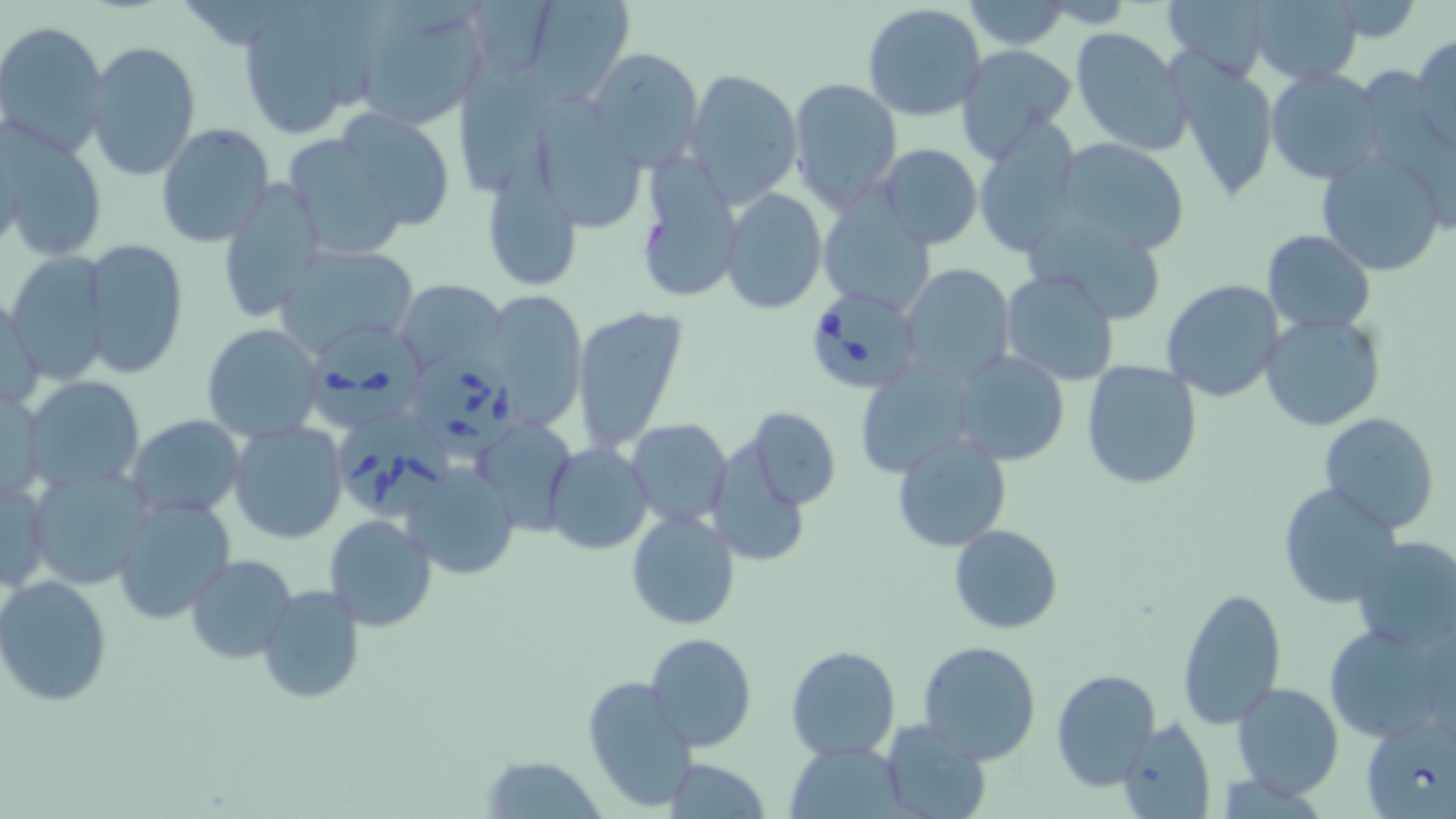

Summary:
  - Coordinate format: approximate bounding boxes as (x1, y1, x2, y2) in pixels
  - Babesia divergens-infected red blood cell locations: (801, 286, 922, 399), (307, 319, 426, 431), (411, 344, 523, 461), (336, 407, 453, 519)
  - Uninfected red blood cell locations: (350, 0, 493, 130), (517, 0, 630, 104), (1160, 0, 1275, 78), (1246, 0, 1363, 85), (235, 1, 380, 138), (964, 1, 1073, 49), (1325, 1, 1424, 45), (862, 3, 987, 122), (0, 21, 111, 158), (1070, 28, 1191, 152), (1411, 34, 1456, 152), (83, 40, 201, 182), (952, 44, 1077, 160), (584, 47, 703, 171), (1168, 53, 1281, 205), (683, 70, 802, 205), (1264, 70, 1384, 184), (787, 76, 903, 210), (334, 109, 456, 231), (154, 123, 274, 249), (1, 124, 108, 261), (971, 124, 1084, 255), (283, 135, 411, 259), (1053, 139, 1191, 256), (877, 145, 983, 249), (1316, 146, 1447, 277), (634, 154, 743, 307), (480, 170, 587, 294), (214, 179, 327, 324), (719, 188, 825, 314), (817, 194, 937, 317), (1025, 212, 1172, 325), (1261, 230, 1375, 335), (78, 239, 189, 378), (274, 243, 418, 359), (3, 249, 111, 382), (901, 262, 1016, 385), (1001, 269, 1119, 387), (393, 279, 506, 375), (1161, 279, 1285, 403), (482, 288, 589, 426), (1, 290, 46, 416), (572, 307, 689, 457), (1259, 311, 1386, 431), (201, 323, 324, 443), (949, 349, 1070, 466), (852, 360, 984, 479), (1081, 360, 1204, 488), (22, 376, 146, 492), (1, 388, 47, 502), (742, 407, 841, 510), (1319, 412, 1440, 534), (124, 413, 247, 520), (473, 414, 579, 531), (625, 418, 733, 527), (226, 420, 349, 545), (892, 431, 1010, 553), (543, 442, 654, 556), (704, 444, 815, 566), (401, 462, 521, 581), (28, 466, 156, 591), (1, 471, 53, 596), (1277, 482, 1403, 608), (357, 493, 506, 617), (109, 498, 237, 625), (626, 511, 741, 629), (323, 513, 438, 632), (949, 524, 1063, 634), (1350, 537, 1456, 652), (186, 554, 298, 666), (0, 575, 117, 706), (256, 583, 367, 705), (1176, 586, 1286, 729), (1323, 621, 1454, 744), (646, 632, 756, 750), (916, 640, 1042, 765), (785, 644, 901, 762), (1049, 670, 1161, 790), (582, 676, 696, 812), (1232, 682, 1344, 798), (1115, 717, 1217, 819), (877, 719, 991, 819), (789, 742, 903, 817), (482, 756, 605, 816), (662, 758, 772, 817)
  - Slide-level diagnosis: Babesia divergens
  - Modality: optical microscopy
  - Image size: 1456×819 pixels
  - Stain: May-Grünwald-Giemsa
  - Preparation: thin blood film
  - Field of view: one of a larger specimen
  - Magnification: 1000x